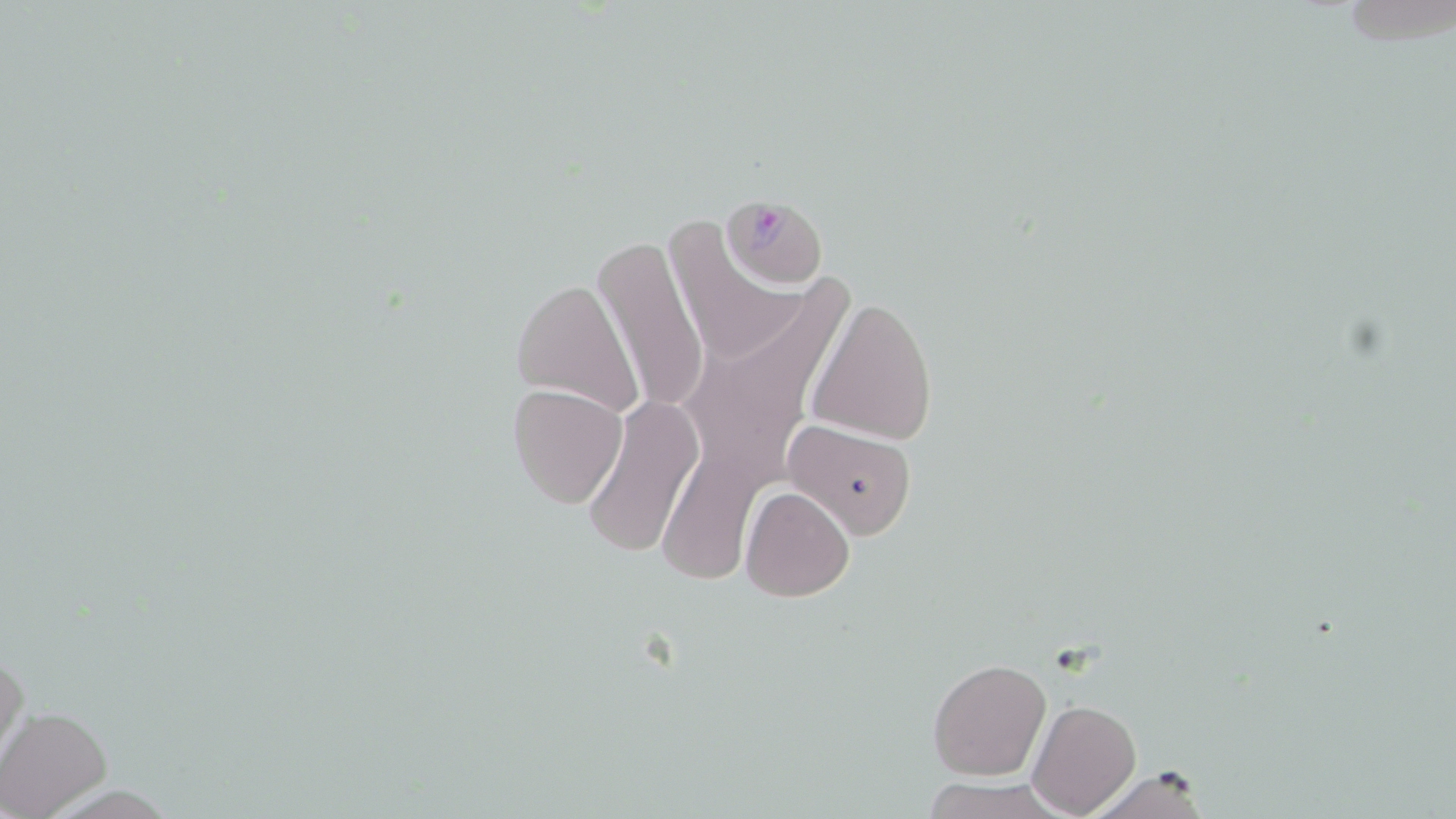

Summary:
  - Coordinate format: approximate bounding boxes as [x1, y1, x2, y2] in pixels
  - Uninfected red blood cell locations: [669, 225, 798, 366], [592, 236, 710, 417], [509, 277, 645, 416], [709, 290, 861, 420], [807, 298, 938, 444], [509, 384, 628, 508], [584, 394, 703, 557], [784, 418, 920, 538], [666, 442, 771, 579], [740, 485, 854, 602], [1, 648, 28, 769], [928, 657, 1051, 780], [1028, 699, 1141, 817], [1, 706, 113, 819], [1076, 765, 1215, 819], [919, 778, 1070, 818]
  - Plasmodium falciparum-infected red blood cell locations: [713, 192, 833, 296]
  - Slide-level diagnosis: Plasmodium falciparum
  - Field of view: single
  - Image size: 1456×819 pixels
  - Preparation: thin blood film
  - Magnification: 1000x
  - Stain: May-Grünwald-Giemsa
  - Modality: light microscopy